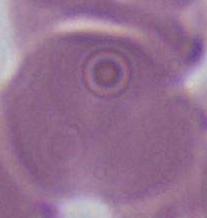
Photomicrograph. Captured at 1000x magnification. A red blood cell is seen.